Assess this cell for malaria.
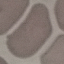

It is uninfected.

Giemsa-stained preparation. Automatically extracted cell patch, resized to 64 × 64 pixels. Thin blood film. Photographed with a smartphone camera at the microscope eyepiece.